Classify this cell by malaria status.
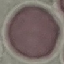
Uninfected.

{
  "image_type": "automatically extracted cell patch, resized to 64 × 64 pixels",
  "preparation": "thin blood film",
  "capture": "smartphone through the microscope eyepiece",
  "stain": "Giemsa"
}